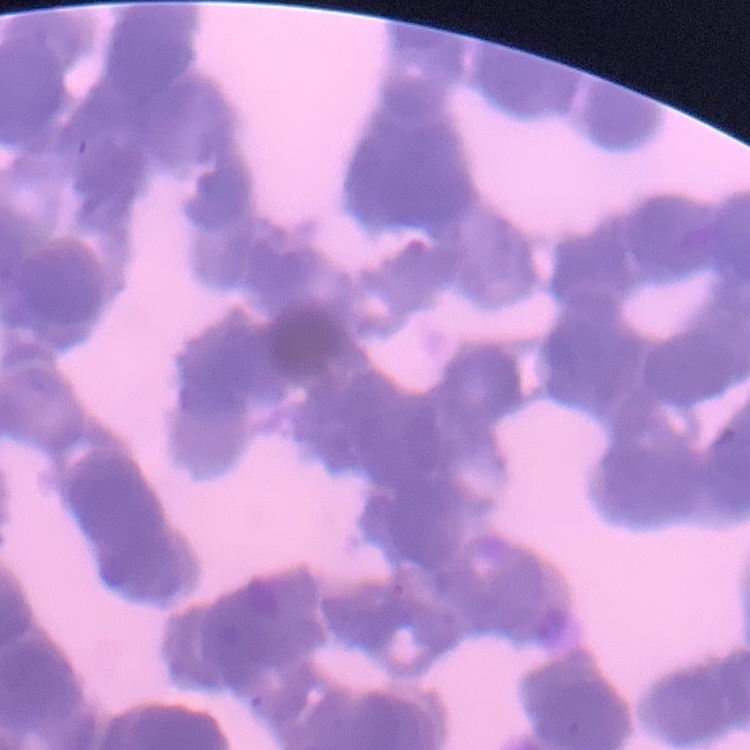
Summary:
  - Erythrocyte morphology: rouleaux formation
  - Stain: Field's or Giemsa
  - Image type: square crop of a larger photomicrograph
  - Preparation: thin peripheral smear